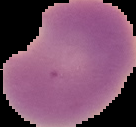
From a thin blood smear. Result: malaria parasites identified. Cell region segmented out of the field of view; the surrounding area is masked to black. Image is 136×127 pixels.